Locate platelets.
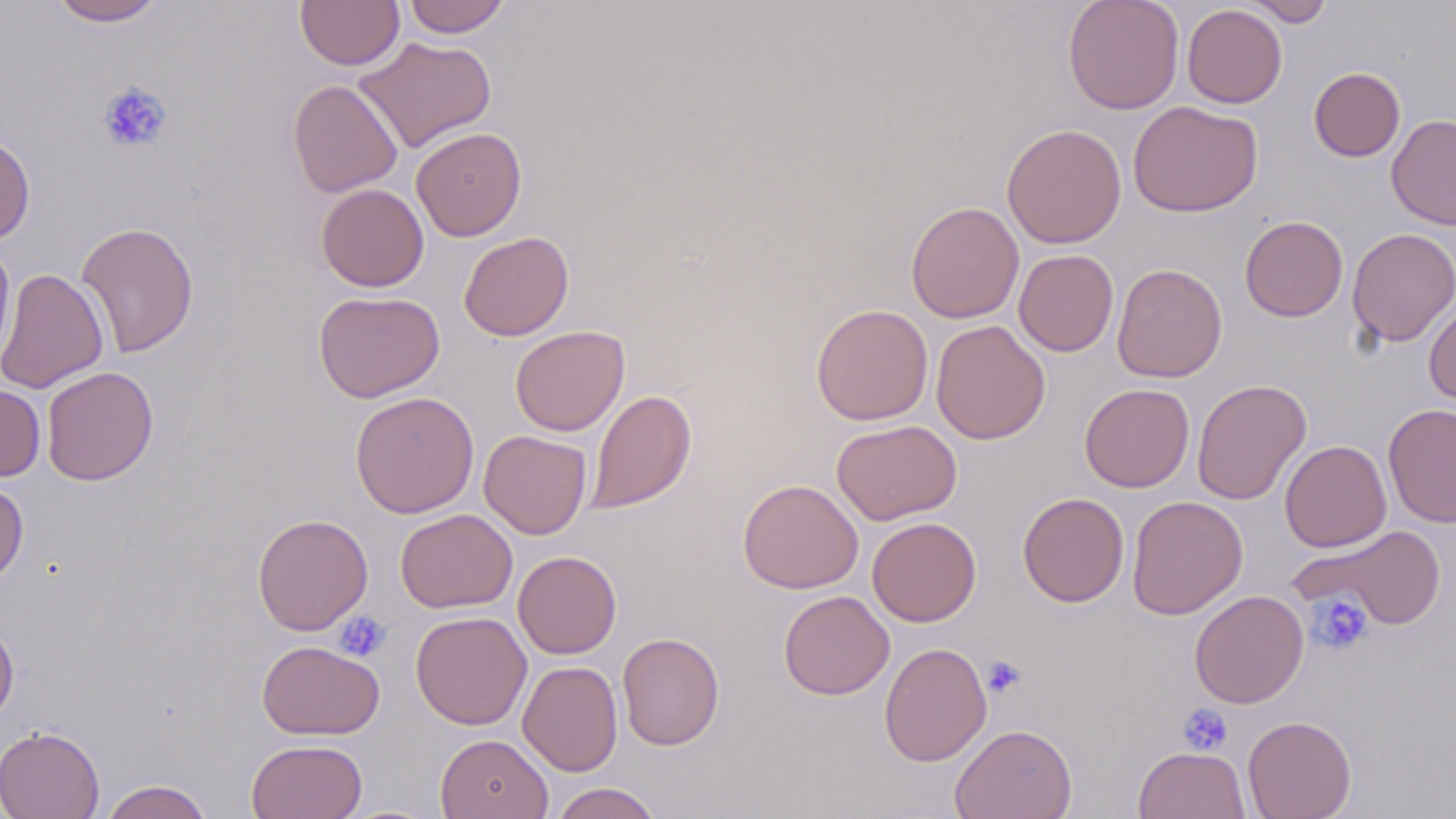
Approximate bounding boxes as named x1/y1/x2/y2 corners in pixels.
Platelets: (x1=98, y1=81, x2=172, y2=153), (x1=1307, y1=593, x2=1373, y2=655), (x1=334, y1=610, x2=391, y2=662), (x1=981, y1=656, x2=1025, y2=699), (x1=1177, y1=702, x2=1233, y2=755).

Summary:
  - Uninfected red blood cell locations: (x1=49, y1=0, x2=167, y2=26), (x1=295, y1=0, x2=405, y2=70), (x1=402, y1=0, x2=511, y2=38), (x1=1062, y1=0, x2=1185, y2=114), (x1=1243, y1=0, x2=1335, y2=26), (x1=1182, y1=4, x2=1287, y2=108), (x1=354, y1=36, x2=496, y2=154), (x1=1309, y1=67, x2=1405, y2=162), (x1=287, y1=78, x2=403, y2=198), (x1=1128, y1=100, x2=1263, y2=218), (x1=1386, y1=114, x2=1456, y2=230), (x1=1002, y1=123, x2=1127, y2=249), (x1=411, y1=127, x2=526, y2=241), (x1=0, y1=132, x2=35, y2=244), (x1=316, y1=183, x2=429, y2=291), (x1=906, y1=201, x2=1025, y2=324), (x1=1239, y1=216, x2=1348, y2=322), (x1=76, y1=221, x2=199, y2=358), (x1=1346, y1=228, x2=1456, y2=347), (x1=459, y1=231, x2=574, y2=341), (x1=0, y1=241, x2=16, y2=366), (x1=1013, y1=249, x2=1119, y2=357), (x1=1112, y1=263, x2=1227, y2=383), (x1=0, y1=267, x2=108, y2=394), (x1=313, y1=290, x2=445, y2=403), (x1=1424, y1=299, x2=1456, y2=410), (x1=810, y1=304, x2=934, y2=425), (x1=931, y1=320, x2=1050, y2=445), (x1=510, y1=325, x2=630, y2=436), (x1=41, y1=366, x2=158, y2=486), (x1=1192, y1=378, x2=1312, y2=506), (x1=1079, y1=383, x2=1195, y2=492), (x1=0, y1=384, x2=46, y2=481), (x1=586, y1=389, x2=697, y2=515), (x1=350, y1=391, x2=480, y2=518), (x1=1383, y1=404, x2=1455, y2=527), (x1=831, y1=419, x2=962, y2=525), (x1=479, y1=430, x2=591, y2=539), (x1=1280, y1=440, x2=1392, y2=552), (x1=0, y1=479, x2=28, y2=585), (x1=738, y1=479, x2=863, y2=594), (x1=1018, y1=492, x2=1129, y2=607), (x1=1126, y1=495, x2=1247, y2=619), (x1=395, y1=508, x2=518, y2=613), (x1=252, y1=513, x2=373, y2=636), (x1=867, y1=517, x2=982, y2=626), (x1=1295, y1=524, x2=1449, y2=630), (x1=513, y1=551, x2=621, y2=659), (x1=1189, y1=589, x2=1309, y2=708), (x1=778, y1=590, x2=895, y2=700), (x1=410, y1=610, x2=531, y2=730), (x1=0, y1=618, x2=19, y2=726), (x1=617, y1=631, x2=724, y2=751), (x1=256, y1=640, x2=385, y2=740), (x1=879, y1=642, x2=992, y2=767), (x1=518, y1=661, x2=623, y2=776), (x1=1242, y1=715, x2=1357, y2=819), (x1=949, y1=723, x2=1078, y2=819), (x1=0, y1=725, x2=105, y2=819), (x1=435, y1=733, x2=553, y2=819), (x1=246, y1=739, x2=367, y2=819), (x1=1133, y1=746, x2=1250, y2=819), (x1=100, y1=779, x2=214, y2=819), (x1=549, y1=783, x2=663, y2=818)
  - Slide-level diagnosis: negative for blood parasites
  - Modality: optical microscopy
  - Image size: 1456×819 pixels
  - Field of view: one of a larger specimen
  - Magnification: 1000x
  - Preparation: thin blood smear
  - Stain: May-Grünwald-Giemsa